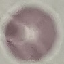

result = negative for malaria parasites
image type = cell patch, automatically extracted from a larger field of view and resized to 64 × 64 pixels
preparation = thin blood smear
capture = smartphone camera at the microscope eyepiece
stain = Giemsa